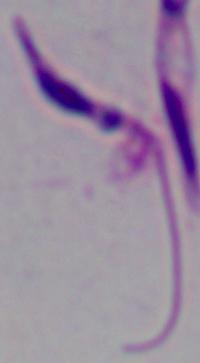
Summary:
  - Modality: micrograph
  - Identification: Leishmania
  - Magnification: 1000x